Locate every blood parasite and identify its species.
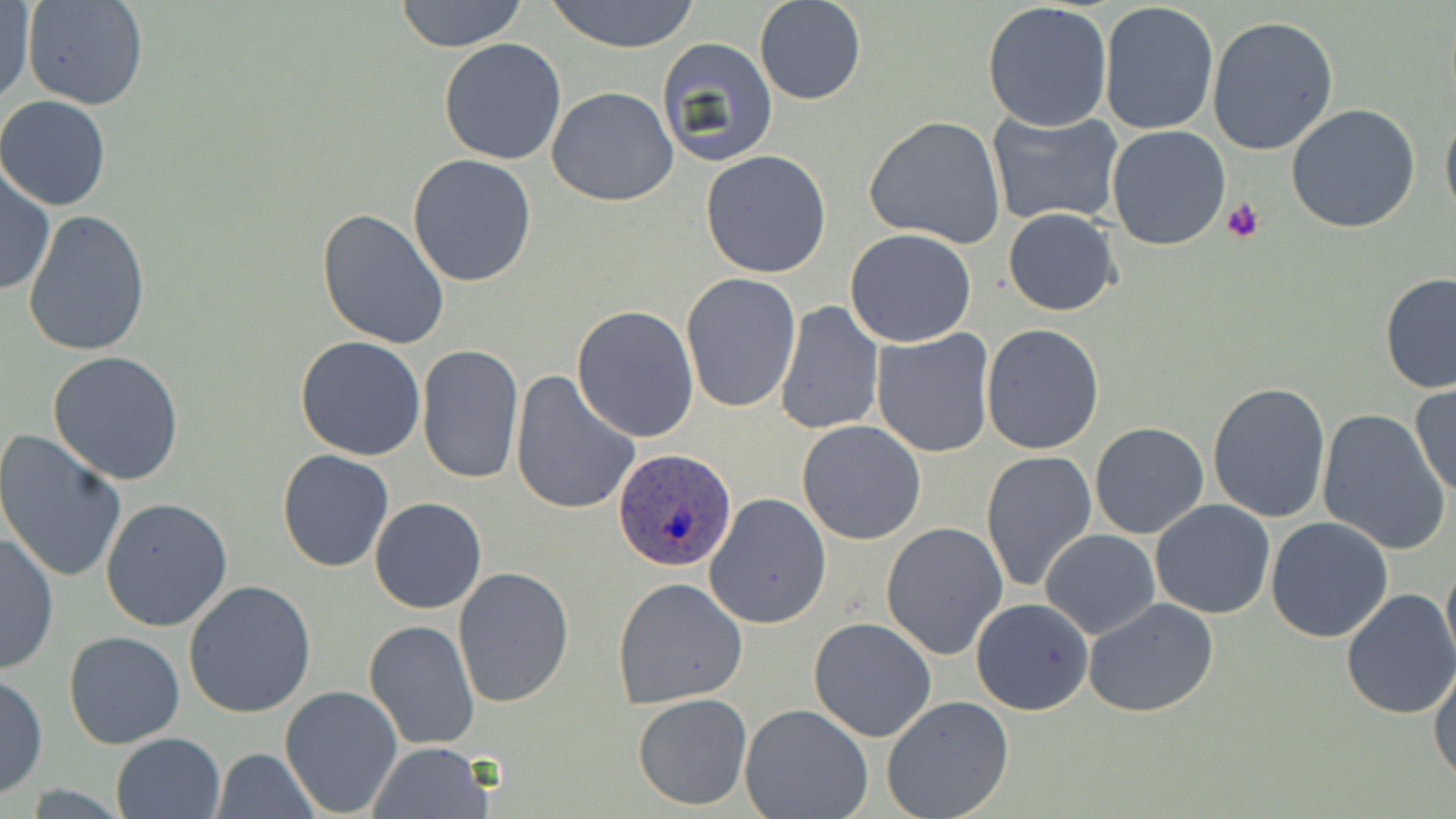

Approximate bounding boxes as [x1, y1, x2, y2] in pixels.
Plasmodium ovale-infected red blood cells: [612, 447, 735, 572].
No Plasmodium falciparum, Plasmodium malariae, Plasmodium vivax, Babesia divergens, or Trypanosoma brucei observed.

Platelet locations: [1222, 198, 1264, 244]. Uninfected red blood cell locations: [394, 0, 528, 51], [543, 0, 702, 52], [754, 0, 867, 105], [19, 1, 149, 111], [1098, 1, 1220, 138], [2, 3, 35, 108], [982, 3, 1114, 133], [1206, 15, 1339, 158], [438, 38, 568, 166], [656, 38, 781, 168], [546, 87, 677, 207], [0, 97, 111, 211], [1286, 103, 1421, 232], [1441, 103, 1456, 231], [986, 109, 1125, 229], [865, 114, 1006, 249], [1106, 125, 1231, 250], [700, 150, 833, 279], [406, 155, 538, 288], [0, 162, 53, 297], [317, 208, 450, 350], [1003, 208, 1120, 316], [23, 209, 151, 356], [845, 228, 978, 348], [1379, 272, 1456, 394], [679, 273, 800, 414], [775, 300, 884, 435], [572, 305, 699, 442], [981, 325, 1105, 454], [872, 330, 997, 460], [294, 336, 426, 460], [416, 343, 523, 486], [48, 351, 186, 485], [511, 371, 640, 517], [1207, 381, 1331, 525], [1409, 382, 1455, 499], [1316, 409, 1451, 555], [796, 420, 927, 545], [1090, 422, 1209, 539], [0, 431, 129, 585], [981, 449, 1097, 592], [277, 450, 393, 572], [704, 493, 832, 629], [101, 496, 233, 632], [370, 497, 488, 614], [1150, 500, 1276, 620], [1266, 517, 1395, 643], [881, 521, 1007, 659], [1040, 529, 1161, 639], [0, 530, 58, 674], [1442, 552, 1455, 672], [453, 565, 575, 707], [612, 576, 748, 708], [183, 581, 316, 720], [1339, 588, 1456, 720], [970, 597, 1094, 715], [1082, 598, 1220, 716], [807, 617, 937, 742], [363, 618, 480, 751], [64, 631, 184, 749], [1430, 663, 1456, 785], [1, 672, 47, 798], [278, 684, 403, 817], [633, 693, 752, 811], [881, 695, 1015, 819], [740, 703, 874, 819], [111, 732, 224, 818], [367, 741, 494, 818], [211, 748, 320, 819]. Slide-level diagnosis: Plasmodium ovale. Image is 1456×819 pixels. May-Grünwald-Giemsa stain. Captured at 1000x magnification. One field of a larger specimen. Optical microscopy. Thin blood film.